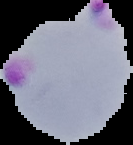

Summary:
  - Result: malaria parasites detected
  - Preparation: thin blood smear
  - Image size: 133×145 pixels
  - Image type: segmented cell region on a black background